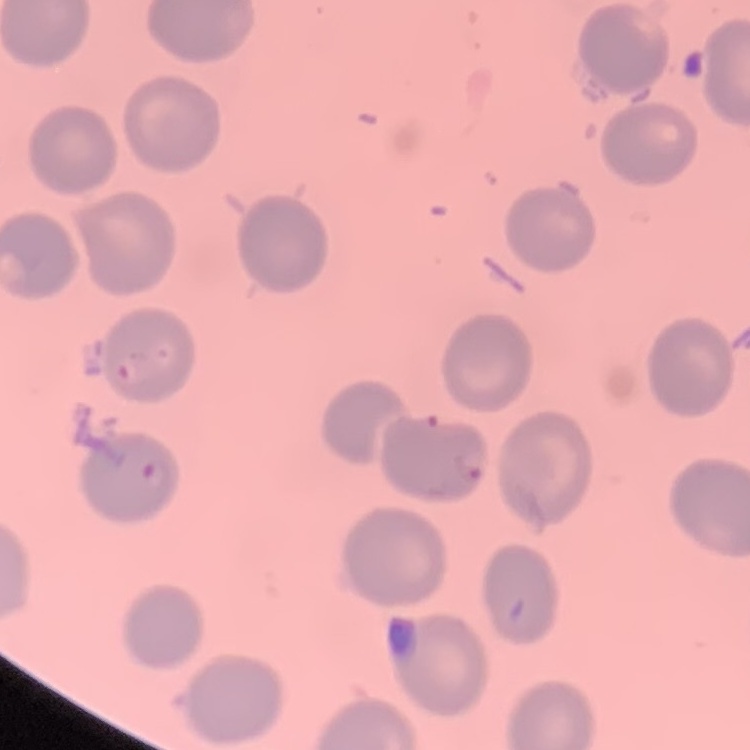
red_blood_cell_morphology: no rouleaux formation
stain: Field's or Giemsa
image_type: square crop of a larger photomicrograph
preparation: thin blood film